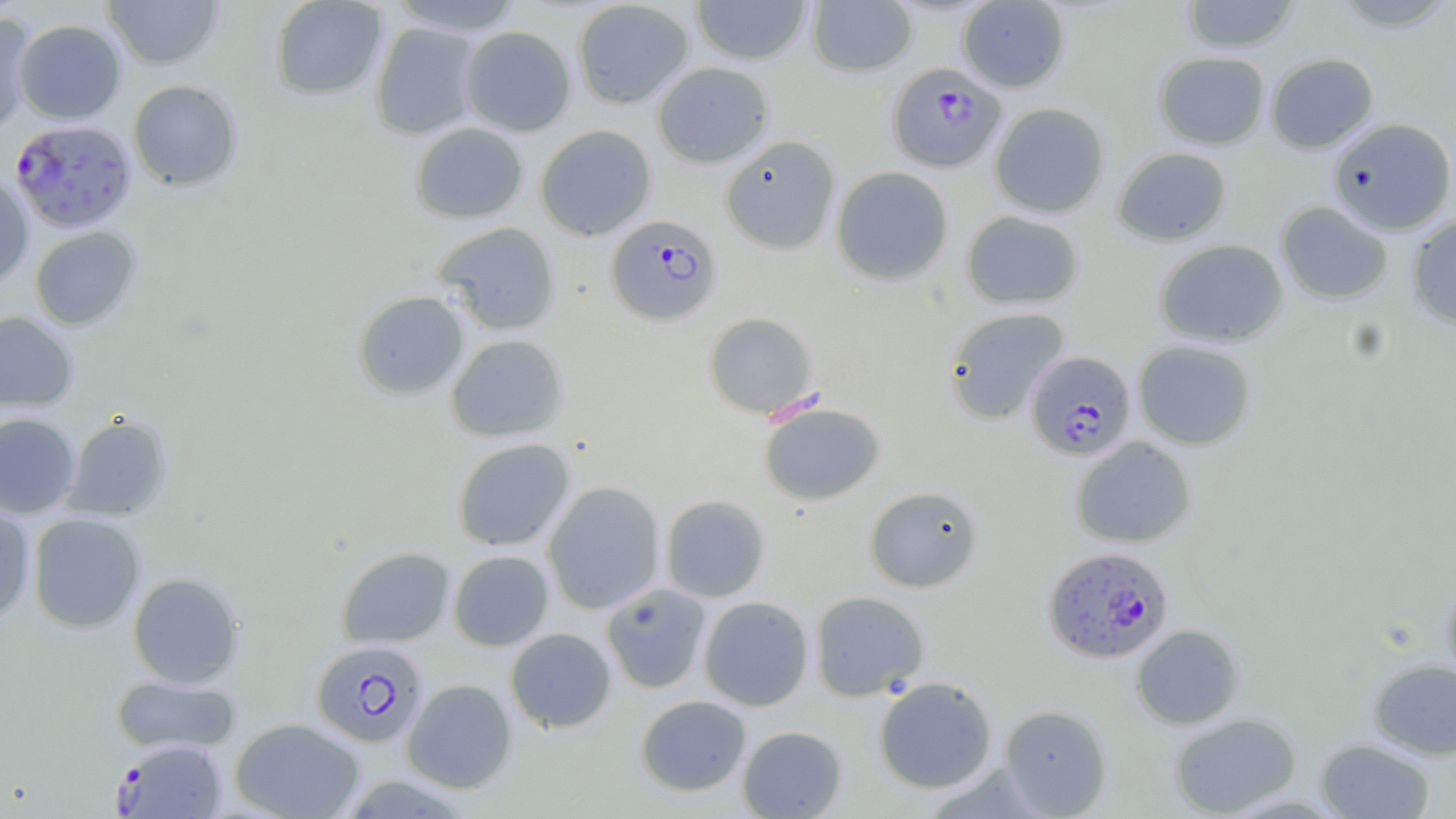
slide-level diagnosis = Plasmodium falciparum
magnification = 1000x
Plasmodium falciparum-infected red blood cell locations = approximate bounding boxes as [x1, y1, x2, y2] in pixels: [888, 63, 1006, 173], [11, 119, 136, 233], [606, 214, 722, 326], [1025, 350, 1137, 460], [1042, 545, 1175, 664], [311, 640, 428, 747], [112, 737, 229, 819]
modality = light microscopy
field of view = single
image size = 1456×819 pixels
uninfected red blood cell locations = approximate bounding boxes as [x1, y1, x2, y2] in pixels: [102, 0, 224, 70], [269, 0, 388, 101], [388, 0, 525, 36], [690, 0, 813, 65], [806, 0, 918, 77], [1179, 0, 1300, 55], [572, 1, 694, 109], [956, 1, 1070, 93], [1327, 1, 1456, 34], [0, 13, 36, 135], [13, 19, 126, 124], [370, 21, 482, 140], [460, 26, 576, 136], [1153, 52, 1270, 150], [1265, 53, 1379, 154], [652, 61, 773, 167], [127, 80, 243, 192], [990, 102, 1109, 218], [1327, 117, 1456, 235], [410, 122, 528, 224], [535, 125, 656, 240], [720, 135, 840, 254], [1112, 147, 1231, 246], [831, 166, 953, 285], [0, 170, 34, 290], [1276, 201, 1393, 304], [961, 210, 1084, 310], [1406, 216, 1456, 329], [434, 221, 562, 335], [29, 226, 142, 331], [1154, 239, 1288, 348], [353, 290, 469, 400], [944, 307, 1070, 424], [0, 310, 79, 413], [704, 312, 818, 419], [445, 334, 569, 442], [1133, 340, 1257, 450], [760, 402, 885, 506], [0, 413, 82, 519], [62, 414, 173, 522], [1071, 436, 1196, 548], [452, 437, 575, 551], [543, 481, 666, 614], [864, 486, 983, 592], [659, 495, 770, 603], [0, 502, 35, 624], [27, 513, 146, 633], [336, 546, 455, 648], [448, 550, 555, 651], [127, 572, 244, 688], [1440, 577, 1456, 691], [601, 583, 711, 694], [810, 590, 929, 701], [698, 595, 814, 711], [1131, 624, 1245, 730], [505, 627, 617, 733], [1368, 659, 1456, 760], [109, 675, 241, 756], [874, 676, 997, 793], [402, 679, 516, 793], [635, 695, 752, 796], [1000, 705, 1112, 817], [1169, 712, 1302, 818], [230, 717, 364, 819], [737, 725, 847, 818], [1316, 739, 1435, 818], [339, 774, 477, 817]
preparation = thin blood smear
stain = May-Grünwald-Giemsa